Assess this cell for malaria.
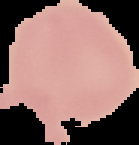

It is uninfected.

Image is 139×145 pixels. The area outside the segmented cell region is set to black. From a thin blood film.